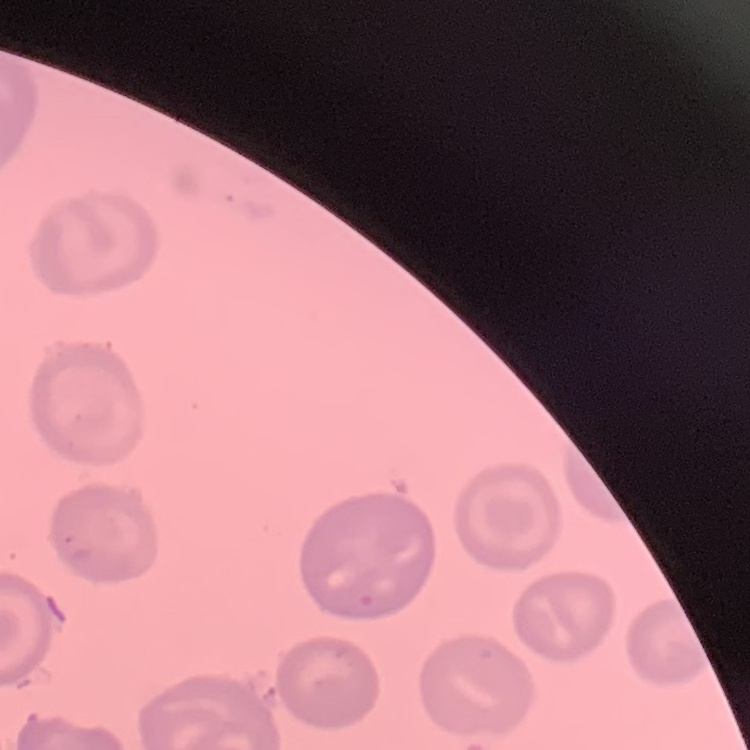
Summary:
  - Erythrocyte morphology: no rouleaux formation
  - Stain: Field's or Giemsa
  - Preparation: thin peripheral smear
  - Image type: square crop of a larger photomicrograph